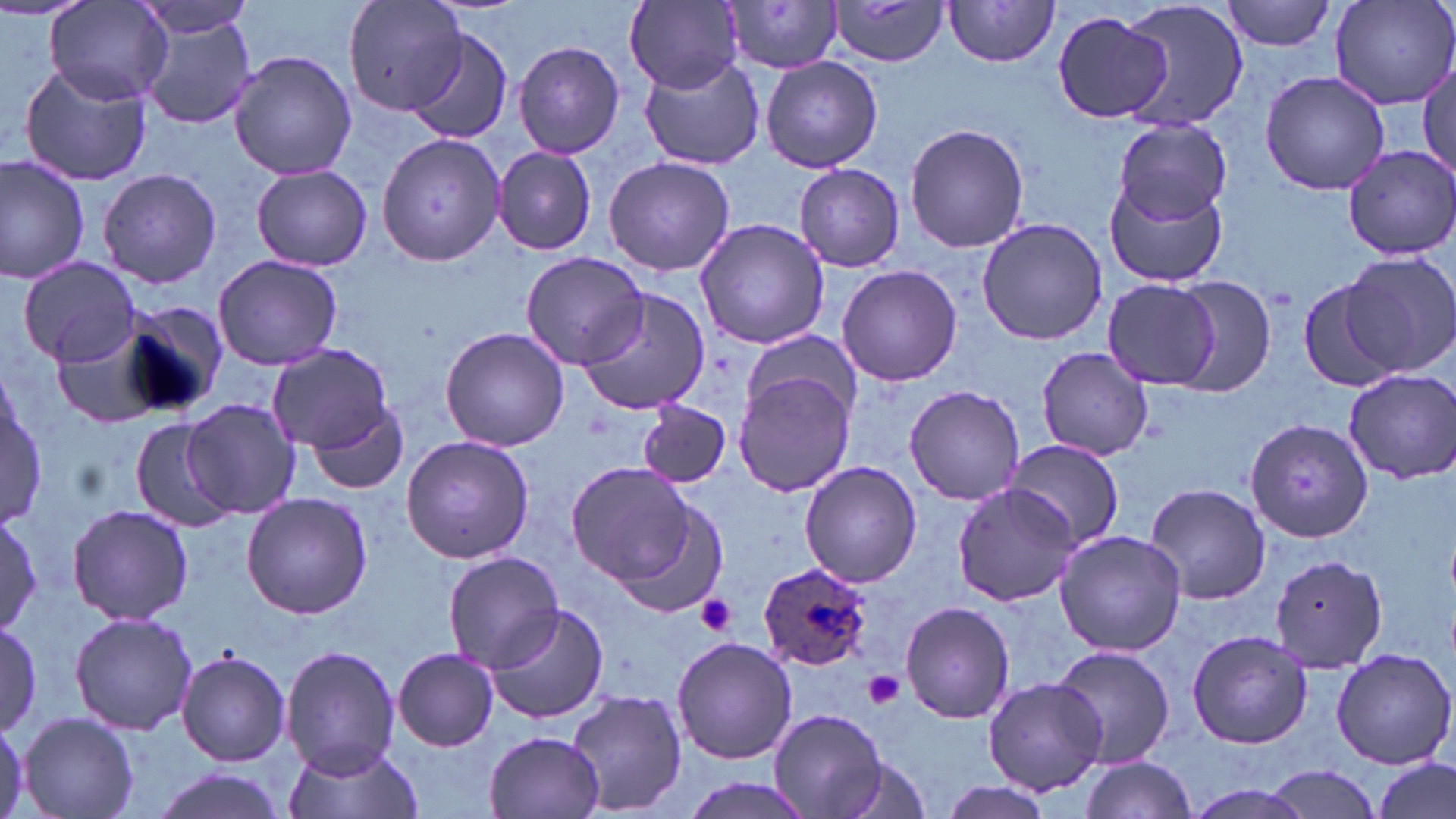

Summary:
  - Coordinate format: approximate bounding boxes as (x1, y1, x2, y2) in pixels
  - Platelet locations: (695, 594, 738, 636), (864, 671, 905, 709)
  - Plasmodium ovale-infected red blood cell locations: (756, 562, 875, 671)
  - Uninfected red blood cell locations: (44, 0, 171, 108), (133, 0, 261, 38), (341, 0, 467, 116), (625, 0, 743, 92), (1117, 0, 1249, 133), (1223, 0, 1340, 52), (1329, 0, 1456, 109), (719, 1, 847, 75), (830, 1, 950, 67), (944, 1, 1062, 70), (1052, 10, 1174, 124), (136, 11, 259, 132), (402, 26, 515, 147), (513, 41, 625, 158), (228, 51, 357, 180), (637, 53, 766, 169), (760, 55, 882, 173), (19, 60, 150, 186), (1417, 66, 1455, 180), (1258, 69, 1392, 194), (626, 73, 754, 252), (1110, 118, 1233, 224), (905, 123, 1030, 253), (376, 132, 507, 267), (1339, 143, 1456, 259), (494, 147, 597, 254), (0, 156, 90, 284), (603, 156, 735, 277), (795, 163, 906, 272), (251, 165, 372, 270), (99, 168, 222, 287), (1104, 177, 1227, 287), (977, 216, 1106, 346), (694, 218, 830, 350), (1339, 250, 1456, 377), (519, 251, 650, 370), (212, 255, 343, 369), (18, 258, 143, 369), (836, 264, 962, 387), (1164, 277, 1278, 394), (1298, 277, 1401, 395), (1101, 279, 1218, 388), (577, 288, 710, 417), (114, 299, 229, 419), (439, 326, 570, 451), (741, 331, 864, 422), (54, 336, 164, 427), (268, 343, 393, 455), (1035, 348, 1153, 462), (1342, 368, 1455, 484), (733, 371, 856, 497), (1, 383, 44, 529), (903, 387, 1025, 503), (184, 397, 299, 518), (307, 402, 409, 495), (636, 402, 732, 488), (129, 418, 235, 533), (1243, 418, 1373, 543), (401, 434, 533, 564), (1008, 441, 1124, 551), (566, 460, 699, 586), (799, 462, 922, 587), (1144, 483, 1271, 606), (951, 484, 1077, 604), (601, 490, 726, 620), (242, 493, 371, 618), (67, 504, 192, 625), (0, 512, 43, 635), (1053, 530, 1186, 657), (443, 552, 563, 670), (1273, 554, 1389, 674), (900, 602, 1016, 722), (485, 603, 609, 724), (68, 610, 198, 735), (0, 620, 43, 736), (1186, 629, 1313, 750), (672, 636, 798, 763), (1052, 645, 1175, 767), (280, 646, 401, 776), (392, 648, 499, 750), (1330, 648, 1455, 769), (175, 649, 293, 767), (983, 676, 1105, 795), (566, 689, 690, 816), (770, 708, 886, 818), (18, 712, 140, 819), (0, 716, 26, 819), (484, 731, 607, 819), (284, 741, 419, 819), (826, 750, 933, 819), (1373, 756, 1452, 819), (1078, 757, 1198, 819), (1257, 766, 1386, 818), (149, 768, 294, 819), (937, 779, 1057, 819), (1180, 781, 1321, 819)
  - Slide-level diagnosis: Plasmodium ovale
  - Stain: May-Grünwald-Giemsa
  - Preparation: thin blood smear
  - Magnification: 1000x
  - Modality: light microscopy
  - Image size: 1456×819 pixels
  - Field of view: one of a larger specimen